Locate every leukocyte (white blood cell).
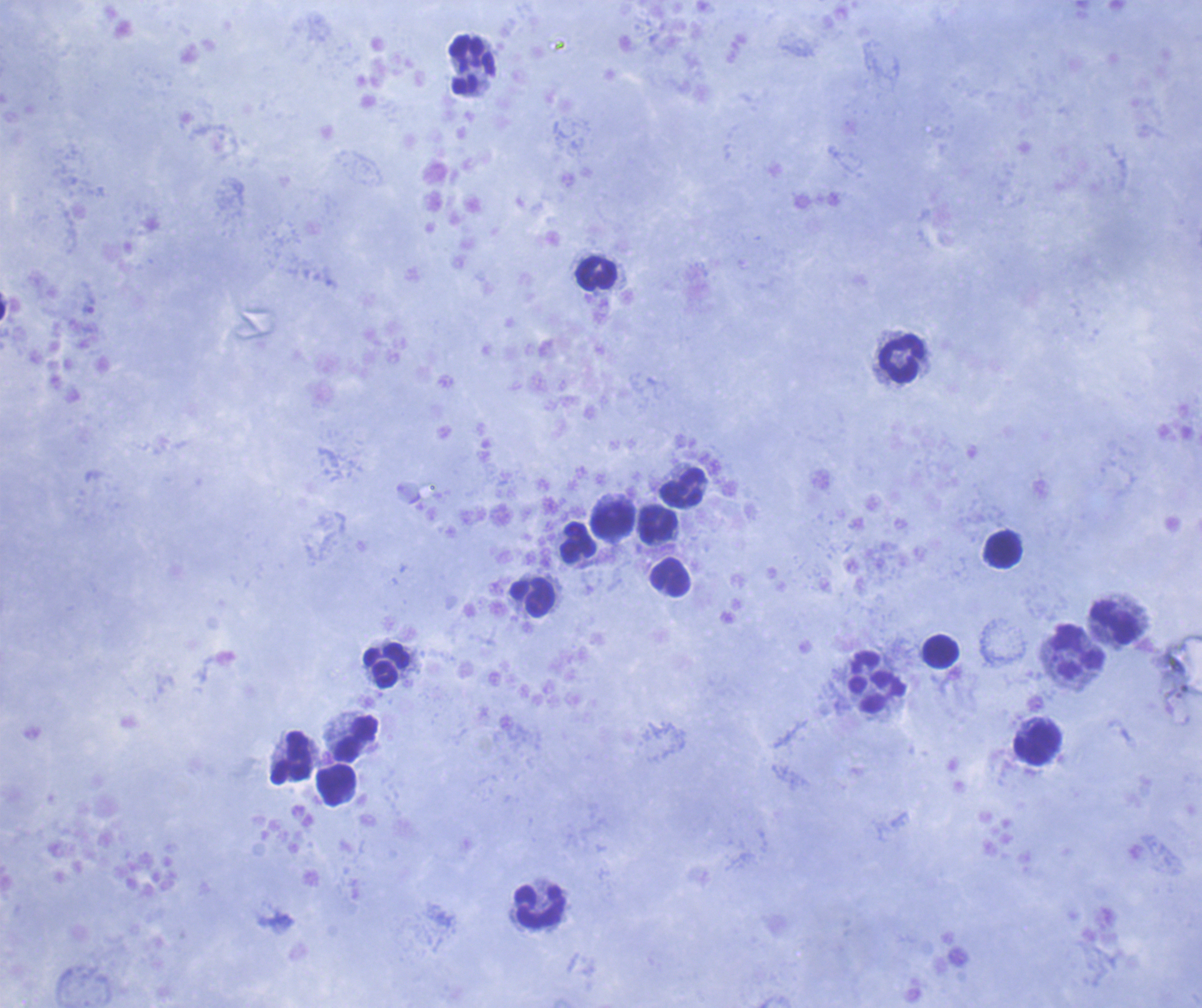

Approximate object centers, in pixels from the top-left corner.
Leukocytes: (x=473, y=65), (x=596, y=273), (x=900, y=360), (x=683, y=488), (x=612, y=520), (x=658, y=524), (x=578, y=542), (x=1003, y=550), (x=670, y=577), (x=532, y=598), (x=1114, y=624), (x=940, y=652), (x=1078, y=652), (x=386, y=665), (x=877, y=694), (x=355, y=738), (x=1035, y=742), (x=290, y=757), (x=335, y=786), (x=539, y=905).

preparation = thick blood film
background quality = satisfactory
stain = Romanowsky
field of view = one from this slide
magnification = 100x
image size = 1202×1008 pixels
result = negative for malaria parasites
context = previously used in an actual diagnosis
coloration quality = good